Name the cell type shown.
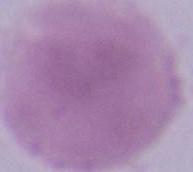
This is an erythrocyte.

Captured at 1000x magnification. Micrograph.